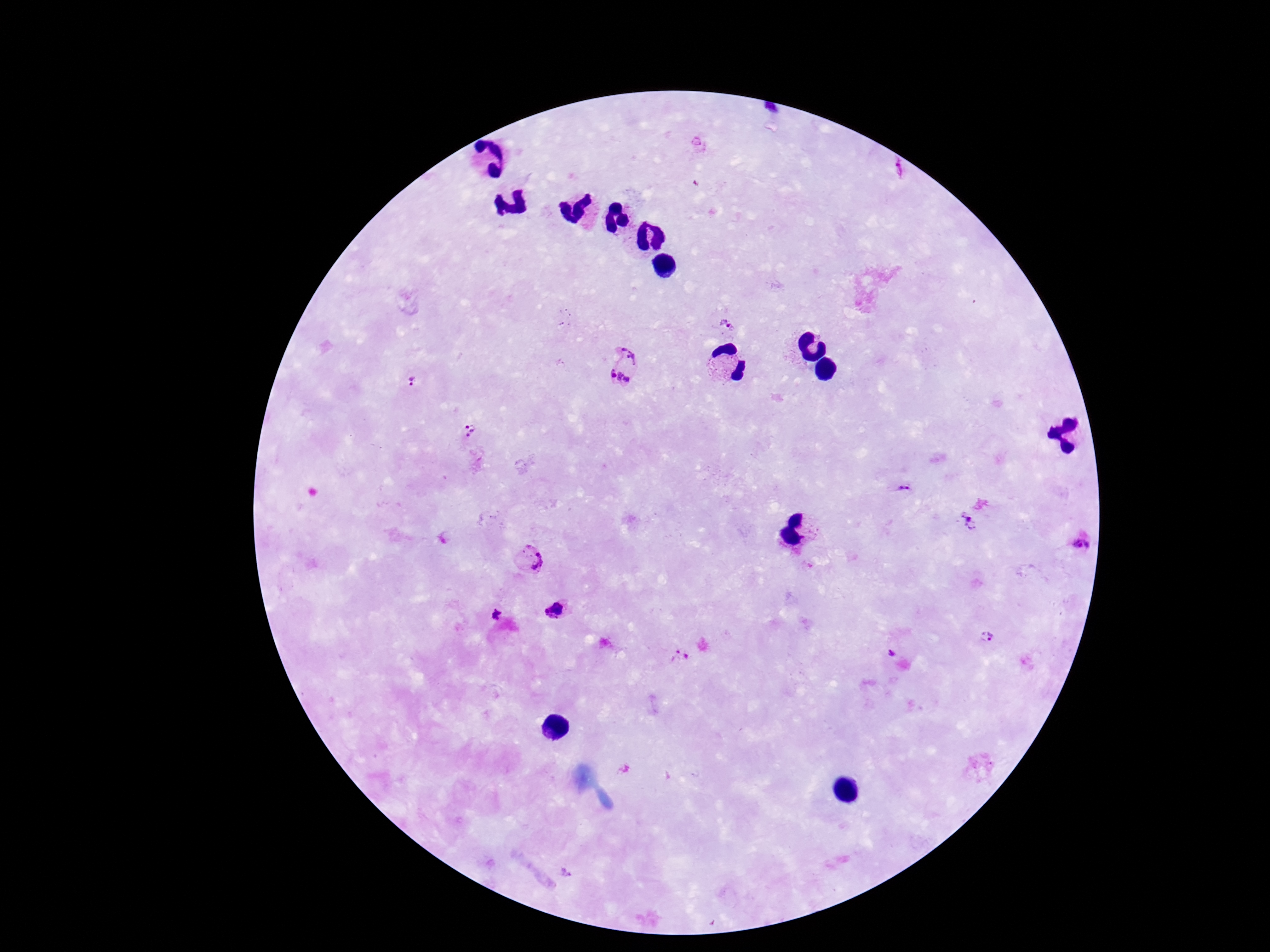
Approximate centers as (x, y) in pixels.
Summary:
  - Plasmodium parasite locations: (897, 169), (727, 322), (625, 366), (414, 381), (469, 433), (906, 487), (965, 523), (1082, 542), (529, 560), (557, 611), (497, 616), (987, 637), (890, 652), (679, 657), (566, 873)
  - Field of view: one from this slide
  - Stain: Giemsa
  - Capture: smartphone camera through the microscope eyepiece
  - Image size: 1270×952 pixels
  - Magnification: 100x
  - Patient malaria status: infected
  - Preparation: thick blood smear